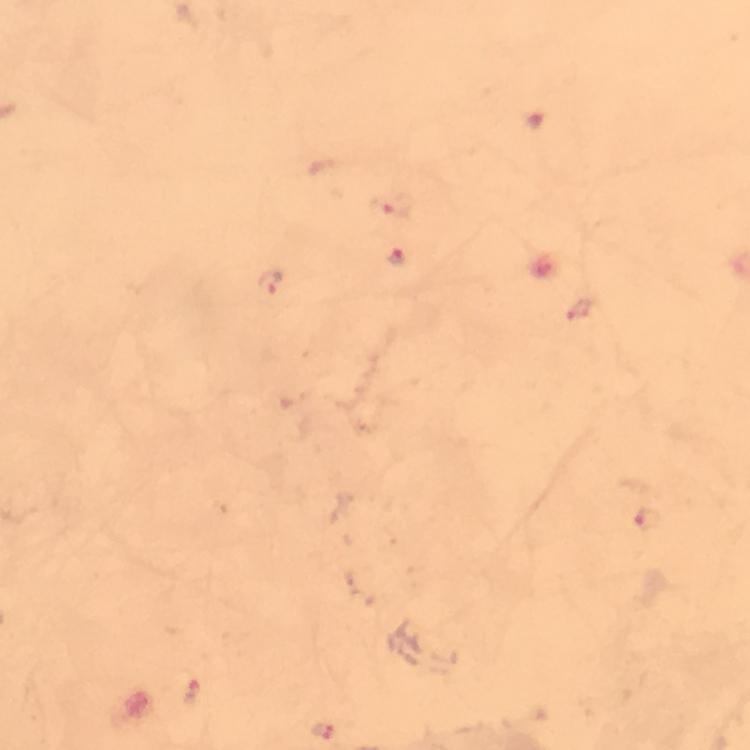 Approximate object centers, in pixels from the top-left corner. Plasmodium parasite locations: (x=394, y=208), (x=397, y=259), (x=269, y=283), (x=647, y=519), (x=192, y=692), (x=321, y=732). 100x magnification. Immersion oil was used. Image is 750×750 pixels. From a diagnostic examination for malaria. Smartphone photograph taken through a microscope. A crop from one field of view. Thick blood smear. Giemsa stain.